Classify this cell by malaria status.
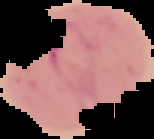

Parasitized.

{
  "image_size": "154×139 pixels",
  "preparation": "thin blood film",
  "image_type": "segmented cell region on a black background"
}